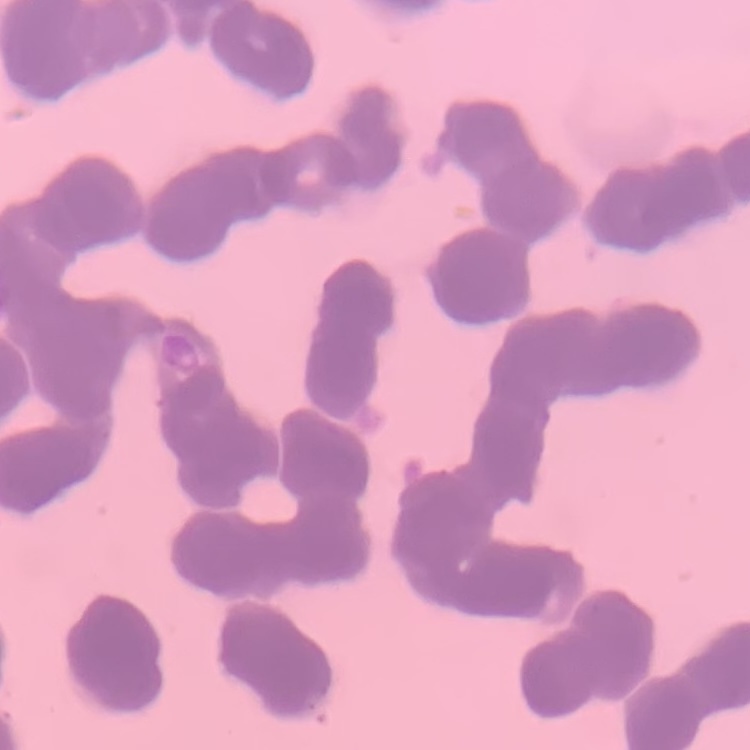 The erythrocytes exhibit rouleaux formation. Field's or Giemsa stain. Thin blood smear. Square crop of a larger photomicrograph.